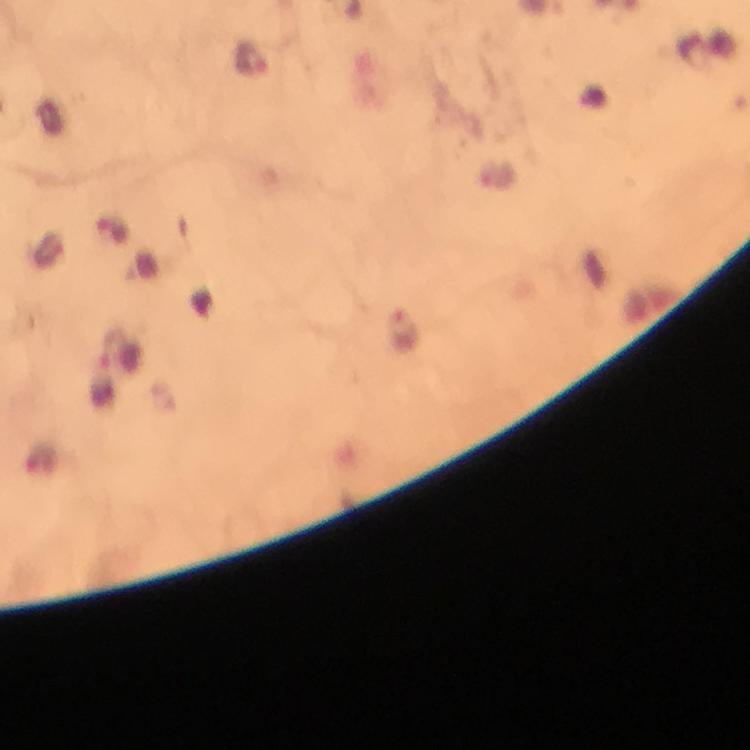
{
  "image_size": "750×750 pixels",
  "capture": "smartphone camera through the microscope",
  "context": "from a diagnostic examination for malaria",
  "stain": "Giemsa",
  "preparation": "thick blood smear",
  "cropped_from": "one field of view",
  "immersion_oil": "applied",
  "magnification": "100x",
  "malaria_parasite_locations": "approximate centers as (x, y) in pixels: (253, 60)"
}